Assess this cell for malaria.
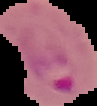
It is parasitized.

Summary:
  - Image type: segmented cell region on a black background
  - Preparation: thin blood film
  - Image size: 97×106 pixels